Name the cell type shown.
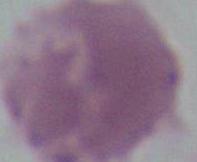
An erythrocyte.

magnification = 1000x
modality = micrograph